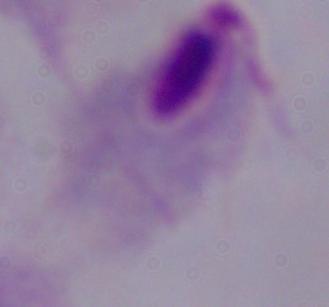 Photomicrograph. Captured at 1000x magnification. A trichomonad is seen.